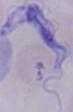
Summary:
  - Modality: micrograph
  - Identification: trypanosome
  - Magnification: 1000x